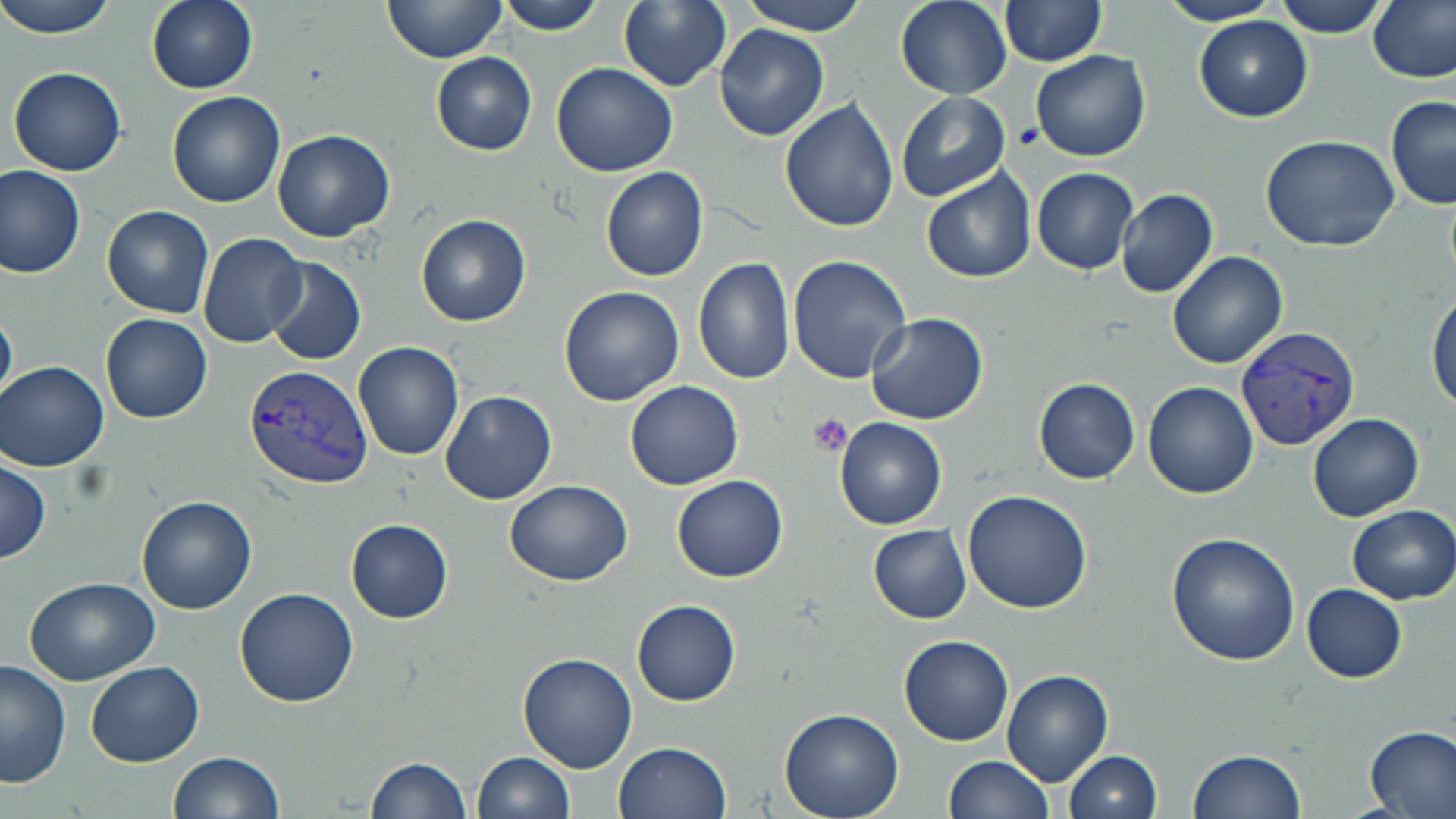

slide-level diagnosis = Plasmodium vivax
field of view = one of a larger specimen
modality = light microscopy
Plasmodium vivax-infected red blood cell locations = approximate bounding boxes as named x1/y1/x2/y2 corners in pixels: (x1=1237, y1=326, x2=1363, y2=448), (x1=244, y1=365, x2=374, y2=490)
platelet locations = approximate bounding boxes as named x1/y1/x2/y2 corners in pixels: (x1=810, y1=413, x2=856, y2=458)
uninfected red blood cell locations = approximate bounding boxes as named x1/y1/x2/y2 corners in pixels: (x1=0, y1=0, x2=120, y2=39), (x1=146, y1=0, x2=257, y2=94), (x1=381, y1=0, x2=507, y2=65), (x1=495, y1=0, x2=607, y2=36), (x1=739, y1=0, x2=870, y2=37), (x1=1156, y1=0, x2=1283, y2=26), (x1=1275, y1=0, x2=1389, y2=38), (x1=1367, y1=0, x2=1456, y2=83), (x1=619, y1=1, x2=731, y2=91), (x1=895, y1=1, x2=1012, y2=100), (x1=999, y1=1, x2=1105, y2=66), (x1=1193, y1=14, x2=1313, y2=122), (x1=714, y1=25, x2=829, y2=143), (x1=1030, y1=50, x2=1150, y2=161), (x1=430, y1=53, x2=537, y2=155), (x1=551, y1=62, x2=678, y2=178), (x1=9, y1=67, x2=126, y2=176), (x1=166, y1=92, x2=286, y2=208), (x1=895, y1=92, x2=1010, y2=203), (x1=1385, y1=94, x2=1456, y2=209), (x1=779, y1=96, x2=899, y2=232), (x1=273, y1=128, x2=395, y2=241), (x1=1259, y1=134, x2=1400, y2=251), (x1=1, y1=165, x2=85, y2=278), (x1=599, y1=166, x2=708, y2=282), (x1=1031, y1=168, x2=1137, y2=275), (x1=920, y1=169, x2=1036, y2=284), (x1=1115, y1=188, x2=1218, y2=299), (x1=101, y1=206, x2=214, y2=317), (x1=416, y1=212, x2=531, y2=327), (x1=196, y1=233, x2=307, y2=350), (x1=1166, y1=250, x2=1288, y2=369), (x1=787, y1=255, x2=912, y2=385), (x1=264, y1=256, x2=366, y2=366), (x1=692, y1=259, x2=795, y2=385), (x1=558, y1=286, x2=685, y2=406), (x1=1426, y1=288, x2=1456, y2=412), (x1=0, y1=302, x2=17, y2=410), (x1=100, y1=313, x2=212, y2=423), (x1=865, y1=313, x2=989, y2=426), (x1=354, y1=342, x2=463, y2=460), (x1=1, y1=360, x2=112, y2=471), (x1=1034, y1=378, x2=1140, y2=484), (x1=625, y1=381, x2=743, y2=490), (x1=1141, y1=382, x2=1258, y2=499), (x1=440, y1=390, x2=557, y2=506), (x1=1307, y1=413, x2=1426, y2=523), (x1=834, y1=417, x2=947, y2=530), (x1=0, y1=459, x2=50, y2=564), (x1=672, y1=476, x2=787, y2=582), (x1=504, y1=479, x2=632, y2=585), (x1=963, y1=489, x2=1092, y2=613), (x1=136, y1=495, x2=256, y2=614), (x1=1347, y1=505, x2=1456, y2=604), (x1=346, y1=518, x2=453, y2=622), (x1=868, y1=524, x2=970, y2=623), (x1=1165, y1=532, x2=1300, y2=666), (x1=23, y1=576, x2=160, y2=685), (x1=1303, y1=584, x2=1406, y2=683), (x1=234, y1=587, x2=358, y2=708), (x1=631, y1=600, x2=740, y2=707), (x1=899, y1=634, x2=1013, y2=746), (x1=516, y1=653, x2=637, y2=773), (x1=0, y1=658, x2=73, y2=790), (x1=84, y1=662, x2=204, y2=767), (x1=1002, y1=670, x2=1114, y2=786), (x1=779, y1=709, x2=904, y2=819), (x1=1363, y1=725, x2=1456, y2=817), (x1=612, y1=741, x2=730, y2=819), (x1=1187, y1=748, x2=1308, y2=818), (x1=170, y1=751, x2=284, y2=819), (x1=472, y1=751, x2=574, y2=818), (x1=1065, y1=751, x2=1162, y2=819), (x1=941, y1=755, x2=1052, y2=819), (x1=365, y1=756, x2=468, y2=819)
magnification = 1000x
image size = 1456×819 pixels
stain = May-Grünwald-Giemsa
preparation = thin blood film